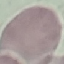

result: no malaria parasites detected
capture: smartphone camera at the microscope eyepiece
stain: Giemsa
image_type: cell patch, automatically extracted from a larger field of view and resized to 64 × 64 pixels
preparation: thin smear